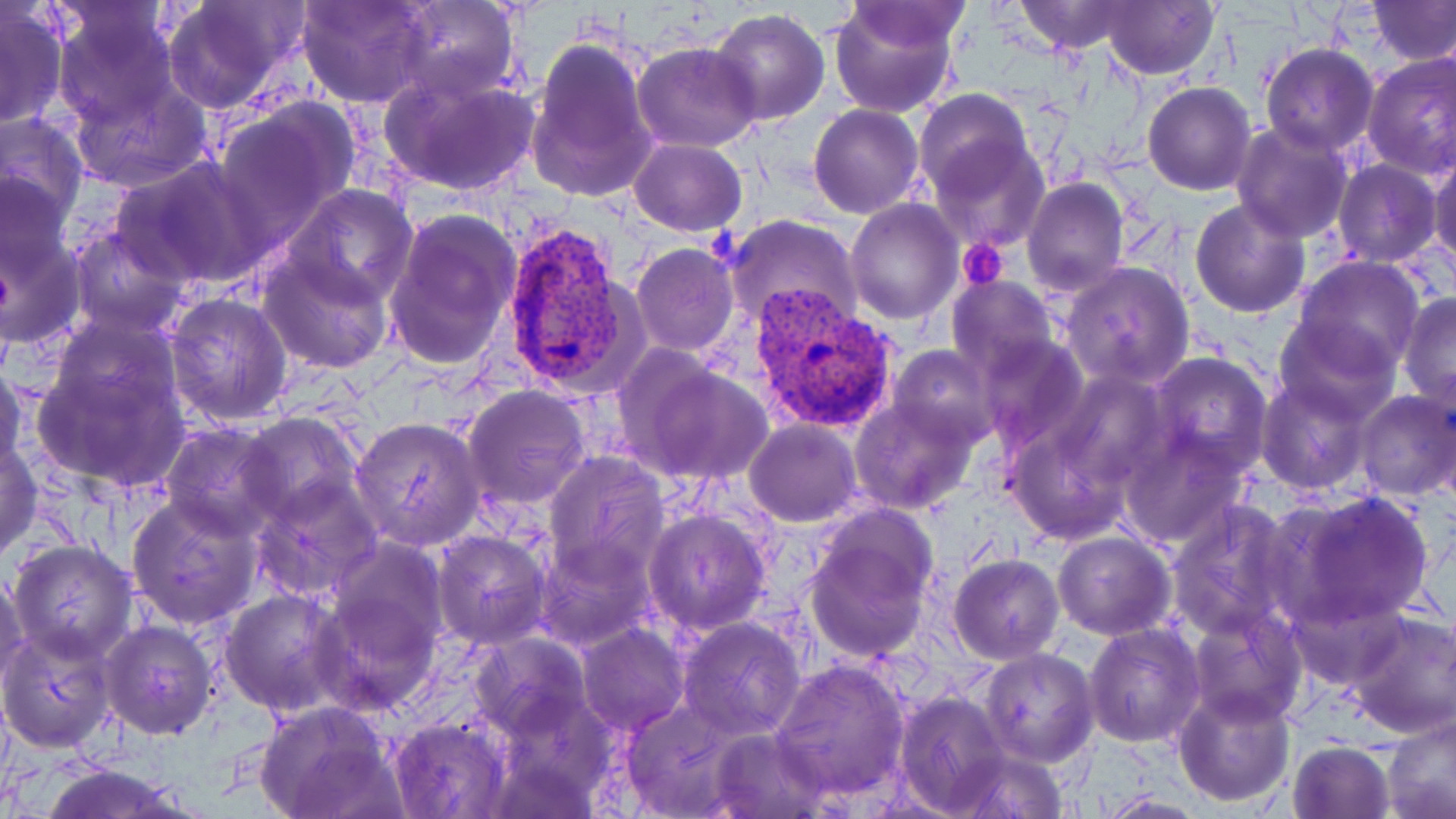

Summary:
  - Coordinate format: approximate bounding boxes as [x1, y1, x2, y2] in pixels
  - Plasmodium vivax-infected red blood cell locations: [498, 219, 639, 398], [750, 288, 899, 436]
  - Platelet locations: [959, 237, 1009, 288]
  - Uninfected red blood cell locations: [160, 0, 307, 112], [297, 0, 435, 108], [391, 0, 520, 104], [829, 0, 961, 117], [1010, 0, 1137, 54], [1101, 0, 1219, 81], [1369, 1, 1456, 65], [1, 2, 69, 128], [48, 3, 185, 129], [710, 9, 829, 127], [527, 38, 657, 200], [633, 41, 764, 150], [1260, 43, 1379, 157], [1362, 51, 1455, 178], [380, 71, 541, 197], [67, 75, 211, 192], [1143, 82, 1255, 195], [913, 88, 1035, 199], [214, 101, 357, 239], [809, 103, 925, 218], [0, 111, 89, 232], [1230, 121, 1354, 242], [628, 138, 746, 236], [934, 144, 1046, 251], [0, 151, 79, 276], [1427, 152, 1455, 272], [115, 156, 267, 287], [1333, 160, 1440, 268], [1022, 176, 1130, 298], [286, 185, 419, 307], [845, 197, 963, 323], [1190, 197, 1310, 318], [0, 206, 88, 352], [382, 210, 521, 373], [724, 213, 863, 330], [68, 228, 191, 338], [631, 244, 739, 358], [257, 248, 395, 373], [1294, 256, 1425, 379], [1061, 261, 1194, 389], [947, 276, 1058, 381], [163, 293, 294, 427], [1397, 293, 1456, 407], [1275, 312, 1400, 422], [47, 313, 182, 426], [975, 332, 1090, 453], [889, 344, 997, 448], [32, 348, 192, 494], [1147, 352, 1273, 476], [626, 356, 775, 487], [0, 360, 29, 483], [1048, 370, 1174, 494], [1256, 373, 1372, 495], [463, 385, 591, 509], [1353, 387, 1456, 502], [850, 396, 979, 514], [240, 412, 362, 523], [351, 416, 485, 550], [1005, 418, 1142, 546], [746, 420, 860, 527], [160, 423, 288, 540], [1120, 432, 1250, 551], [1, 437, 43, 561], [543, 451, 669, 581], [250, 475, 381, 600], [1275, 490, 1436, 629], [126, 495, 263, 630], [1164, 499, 1300, 641], [643, 508, 773, 636], [803, 528, 934, 662], [432, 531, 552, 649], [1053, 532, 1176, 639], [327, 538, 449, 656], [8, 539, 137, 664], [536, 540, 655, 652], [949, 553, 1064, 664], [0, 567, 29, 691], [220, 588, 348, 715], [1285, 590, 1407, 693], [315, 591, 439, 713], [1186, 607, 1307, 726], [1342, 609, 1455, 741], [99, 618, 218, 738], [677, 618, 804, 738], [1082, 623, 1204, 748], [577, 624, 688, 735], [0, 625, 119, 751], [472, 632, 591, 736], [981, 649, 1100, 768], [769, 657, 912, 802], [1172, 686, 1296, 807], [893, 690, 1010, 816], [618, 695, 743, 816], [255, 702, 400, 819], [1382, 709, 1456, 819], [388, 715, 510, 819], [706, 729, 832, 818], [1286, 740, 1396, 819], [948, 744, 1071, 818], [33, 763, 195, 819], [1091, 792, 1210, 818]
  - Slide-level diagnosis: Plasmodium vivax
  - Image size: 1456×819 pixels
  - Modality: light microscopy
  - Magnification: 1000x
  - Stain: May-Grünwald-Giemsa
  - Preparation: thin blood smear
  - Field of view: single